Name the parasite shown.
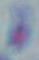
This is Toxoplasma gondii.

1000x magnification. Photomicrograph.